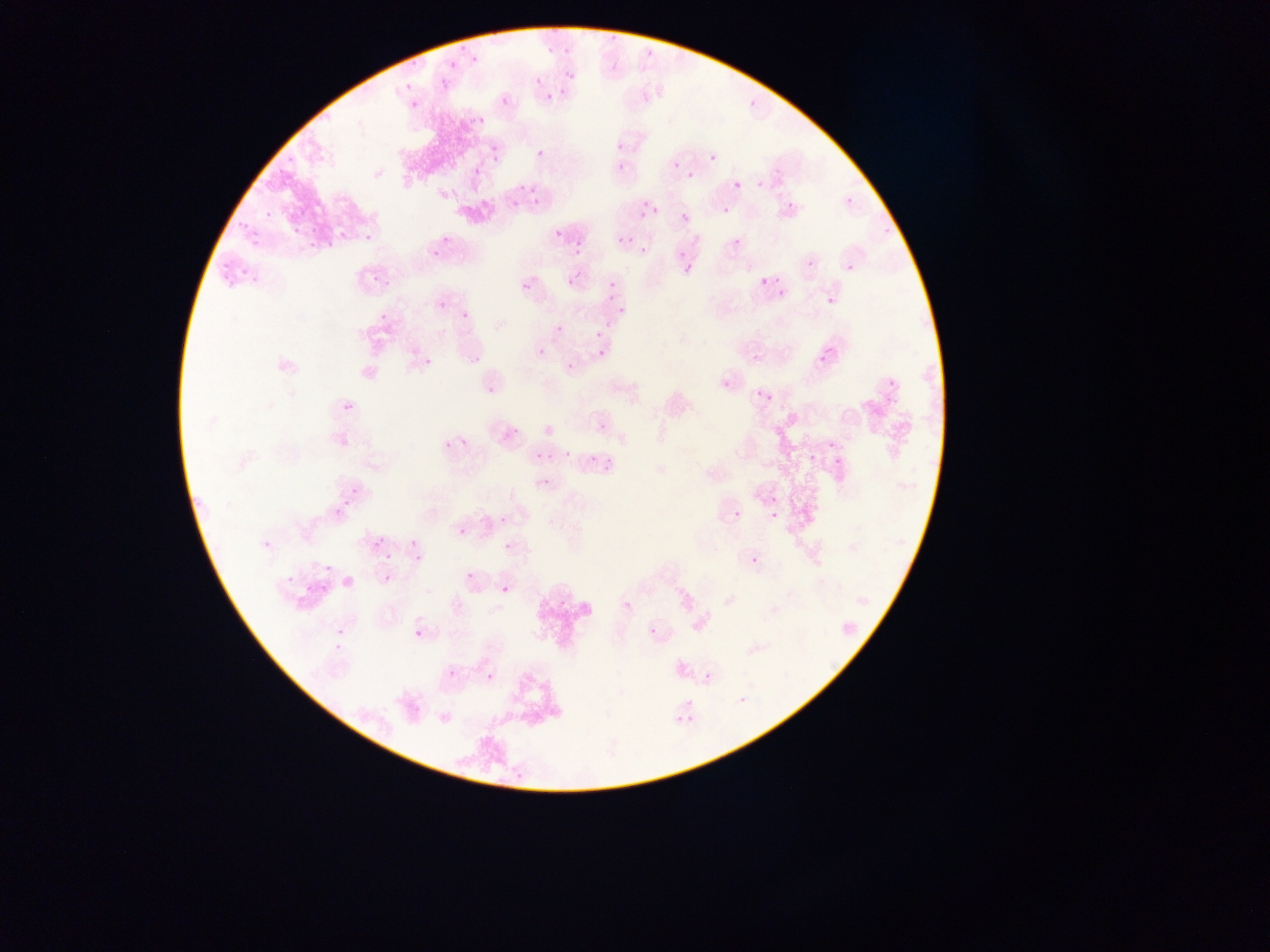

country = Ghana
preparation = thin blood smear
malaria parasite locations = approximate bounding boxes as (left, top, right, bottom) in pixels: (466, 53, 479, 73), (407, 54, 424, 68), (444, 59, 463, 73), (559, 69, 576, 81), (399, 78, 415, 88), (436, 78, 453, 92), (555, 89, 574, 97), (542, 91, 552, 108), (409, 93, 423, 107), (501, 96, 509, 105), (750, 96, 763, 106), (466, 113, 480, 130), (491, 144, 501, 153), (535, 147, 546, 157), (488, 153, 497, 165), (705, 155, 718, 167), (273, 160, 292, 180), (671, 161, 679, 169), (618, 162, 625, 171), (474, 166, 482, 175), (681, 167, 692, 180), (754, 179, 770, 189), (734, 181, 742, 189), (530, 184, 539, 208), (517, 185, 526, 192), (847, 197, 854, 205), (511, 199, 519, 207), (783, 201, 797, 208), (262, 206, 273, 225), (651, 207, 659, 215), (722, 207, 730, 215), (234, 208, 251, 231), (681, 214, 689, 222), (251, 221, 268, 250), (550, 223, 561, 236), (361, 225, 371, 242), (878, 226, 890, 242), (288, 228, 298, 234), (302, 231, 323, 250), (575, 232, 587, 245), (325, 233, 348, 253), (621, 237, 630, 245), (732, 238, 743, 247), (426, 243, 438, 256), (210, 248, 235, 275), (572, 248, 585, 256), (640, 248, 648, 255), (678, 252, 695, 276), (797, 260, 818, 270), (843, 260, 855, 274), (566, 265, 585, 285), (243, 272, 258, 282), (767, 272, 782, 285), (607, 274, 621, 288), (370, 275, 395, 291), (759, 278, 768, 287), (221, 279, 236, 293), (522, 282, 531, 291), (608, 288, 616, 298), (777, 289, 785, 297), (822, 291, 839, 311), (432, 297, 444, 312), (376, 305, 389, 319), (616, 306, 624, 314), (457, 311, 471, 327), (603, 317, 610, 327), (554, 324, 562, 332), (595, 331, 603, 339), (538, 348, 546, 357), (598, 350, 606, 358), (814, 352, 831, 369), (467, 353, 481, 363), (427, 354, 436, 366), (751, 354, 761, 363), (567, 364, 575, 372), (883, 366, 896, 388), (715, 367, 736, 386), (484, 379, 500, 395), (755, 390, 764, 399), (768, 395, 776, 403), (340, 399, 354, 414), (882, 399, 897, 409), (594, 416, 612, 431), (500, 428, 520, 442), (338, 434, 352, 449), (821, 436, 834, 450), (439, 437, 453, 450), (460, 437, 469, 446), (585, 445, 605, 463), (602, 445, 634, 472), (564, 451, 572, 459), (804, 452, 816, 464), (535, 453, 543, 461), (830, 453, 840, 468), (539, 477, 549, 486), (345, 481, 362, 498), (188, 492, 207, 511), (768, 497, 776, 506), (335, 502, 348, 515), (334, 507, 344, 517), (734, 510, 743, 519), (769, 512, 777, 521), (500, 516, 507, 524), (458, 526, 467, 536), (261, 531, 278, 550), (372, 537, 383, 547), (504, 543, 513, 551), (385, 552, 394, 562), (414, 554, 423, 564), (750, 556, 759, 566), (325, 561, 333, 576), (465, 571, 474, 580), (284, 573, 293, 590), (297, 573, 311, 601), (319, 578, 338, 600), (501, 585, 509, 593), (555, 591, 571, 612), (622, 600, 632, 611), (332, 613, 346, 654), (648, 627, 658, 637), (414, 629, 423, 637), (444, 666, 454, 674), (486, 673, 494, 682), (704, 673, 711, 681), (670, 711, 688, 731), (513, 763, 530, 784) | approximate (x, y) pixel centers of objects too small to bound: (537, 80), (620, 146), (641, 216), (742, 700)
capture = mobile-phone photograph through a microscope
image size = 1270×952 pixels
field of view = single